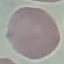

malaria status = uninfected
image type = cell patch, automatically extracted from a larger field of view and resized to 64 × 64 pixels
capture = smartphone through the microscope eyepiece
stain = Giemsa
preparation = thin blood smear